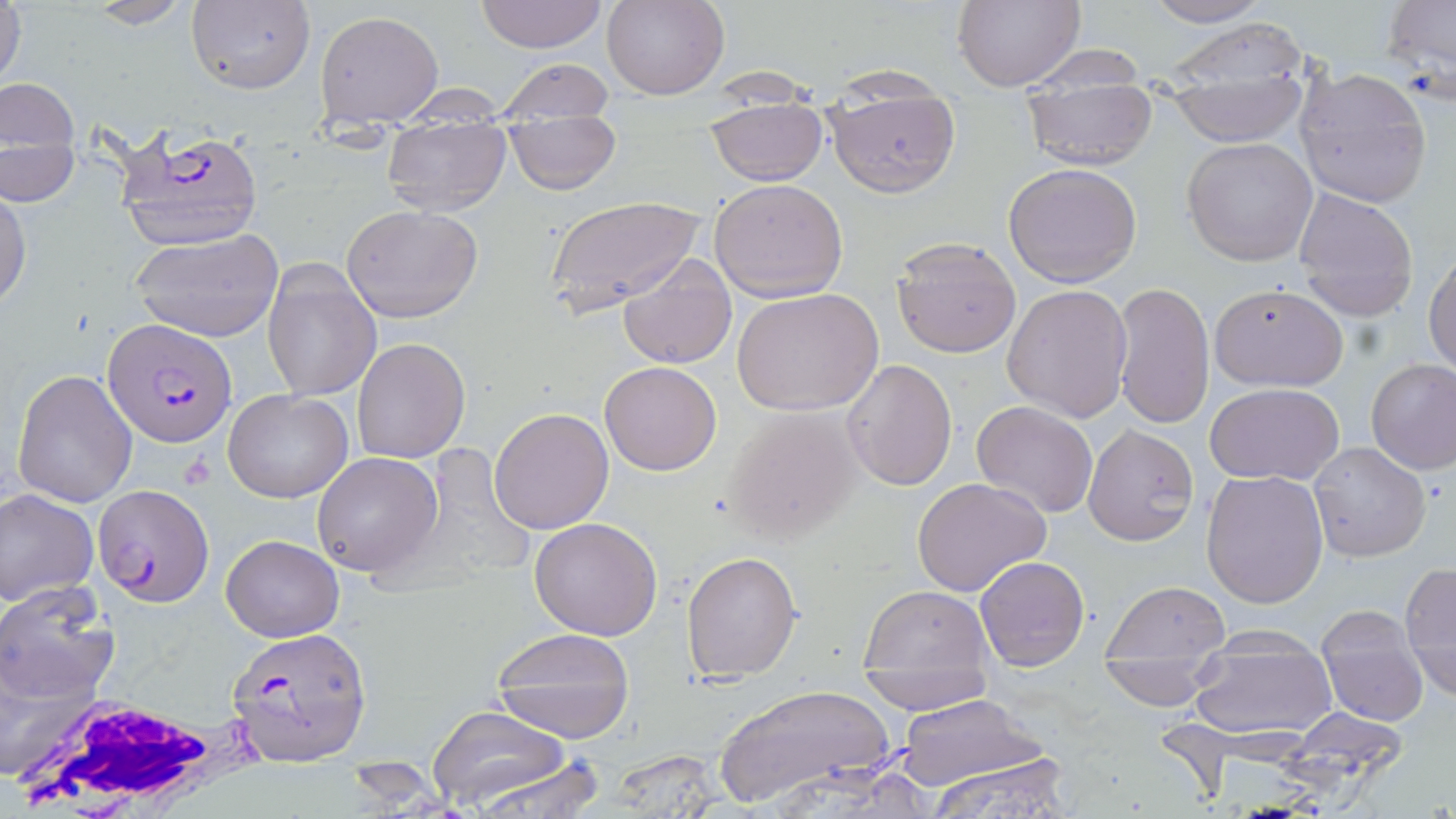
Approximate bounding boxes as (x1,y1)-(x2,y2) corner pairs in pixels. Uninfected red blood cell locations: (1,0)-(27,95), (473,0)-(610,52), (604,0)-(728,100), (1140,0)-(1279,27), (78,1)-(199,28), (184,1)-(316,94), (951,1)-(1084,90), (1380,1)-(1455,97), (316,9)-(444,124), (1159,16)-(1315,91), (1020,43)-(1148,92), (492,56)-(617,121), (1295,67)-(1432,206), (1166,68)-(1308,145), (1,73)-(82,185), (1023,85)-(1159,170), (705,98)-(828,185), (828,99)-(960,198), (382,122)-(511,215), (505,122)-(623,196), (1183,137)-(1316,266), (1,139)-(81,205), (1003,163)-(1142,286), (710,178)-(848,302), (0,189)-(30,309), (1294,190)-(1418,321), (547,195)-(702,316), (341,205)-(483,323), (128,227)-(284,343), (891,237)-(1022,358), (1424,248)-(1456,374), (616,251)-(740,369), (262,262)-(382,400), (1111,281)-(1216,430), (1209,282)-(1350,392), (1002,283)-(1132,422), (731,288)-(883,417), (352,338)-(469,463), (842,358)-(957,491), (1367,359)-(1456,475), (598,361)-(723,475), (11,368)-(139,508), (1205,382)-(1346,486), (222,388)-(354,503), (971,401)-(1098,518), (723,405)-(863,544), (488,408)-(614,534), (1083,423)-(1198,543), (1309,441)-(1432,562), (311,451)-(442,578), (1201,469)-(1330,607), (911,476)-(1052,597), (0,488)-(98,607), (530,517)-(663,640), (221,534)-(344,640), (682,551)-(801,683), (973,555)-(1089,671), (1400,561)-(1456,702), (0,579)-(117,708), (1103,581)-(1229,659), (859,583)-(993,675), (1316,608)-(1429,727), (490,626)-(637,745), (1185,652)-(1338,744), (1099,660)-(1226,711), (859,670)-(996,711), (715,684)-(896,810), (895,693)-(1052,794), (427,706)-(575,810), (923,747)-(1078,818), (603,748)-(730,815), (464,751)-(608,817). Plasmodium falciparum-infected red blood cell locations: (116,126)-(268,251), (102,319)-(235,446), (91,484)-(215,606), (224,626)-(372,767). White blood cell locations: (9,690)-(265,818). Slide-level diagnosis: Plasmodium falciparum. Captured at 1000x magnification. Optical microscopy. May-Grünwald-Giemsa stain. Image is 1456×819 pixels. Single field of view. Thin blood film.